Assess this cell for malaria.
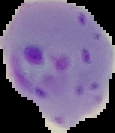
Parasitized.

image size = 115×133 pixels
image type = cell region segmented out of the field of view; surrounding area masked to black
preparation = thin blood film